Assess this cell for malaria.
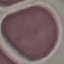

Uninfected.

Giemsa-stained preparation. Acquired by smartphone through the microscope eyepiece. Thin smear of blood. Automatically extracted cell patch, resized to 64 × 64 pixels.